Name the parasite shown.
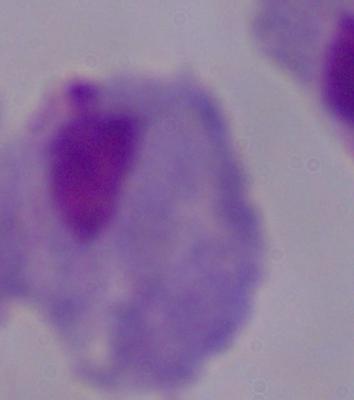

A trichomonad.

Micrograph. Captured at 1000x magnification.